Outline each uninfected red blood cell.
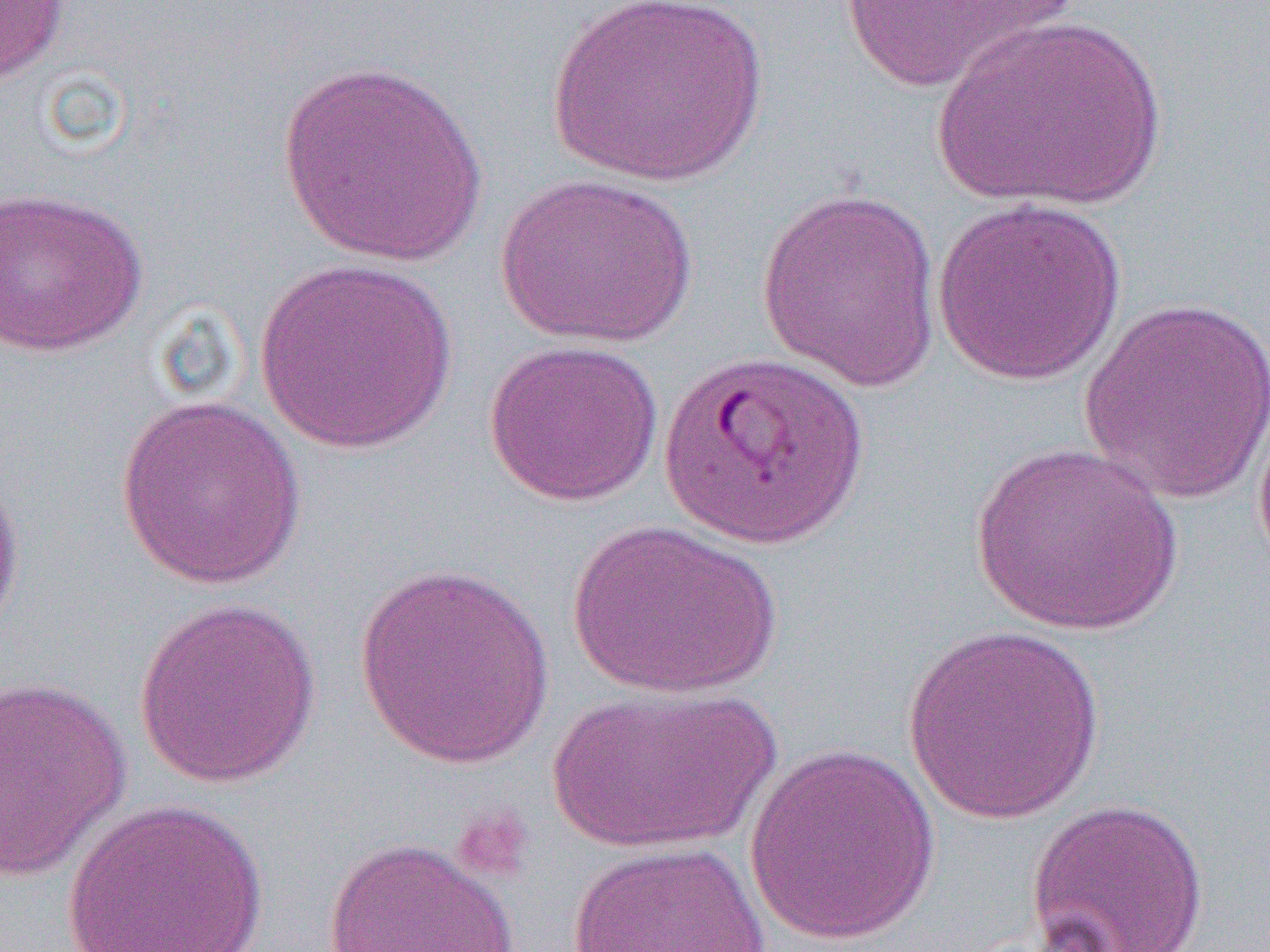

Approximate bounding boxes as named x1/y1/x2/y2 corners in pixels.
Uninfected red blood cells: (x1=0, y1=0, x2=71, y2=88), (x1=546, y1=0, x2=769, y2=186), (x1=833, y1=0, x2=1080, y2=95), (x1=932, y1=15, x2=1167, y2=211), (x1=274, y1=60, x2=493, y2=267), (x1=495, y1=172, x2=699, y2=349), (x1=0, y1=185, x2=149, y2=357), (x1=756, y1=188, x2=942, y2=391), (x1=931, y1=196, x2=1127, y2=387), (x1=253, y1=259, x2=459, y2=454), (x1=1078, y1=295, x2=1270, y2=505), (x1=484, y1=339, x2=665, y2=507), (x1=1251, y1=388, x2=1270, y2=587), (x1=114, y1=393, x2=309, y2=589), (x1=970, y1=442, x2=1186, y2=636), (x1=0, y1=463, x2=25, y2=645), (x1=566, y1=518, x2=783, y2=698), (x1=353, y1=562, x2=556, y2=769), (x1=134, y1=596, x2=323, y2=790), (x1=901, y1=624, x2=1109, y2=824), (x1=0, y1=676, x2=132, y2=883), (x1=546, y1=685, x2=778, y2=854), (x1=743, y1=745, x2=941, y2=947), (x1=1024, y1=797, x2=1211, y2=951), (x1=61, y1=799, x2=270, y2=952), (x1=322, y1=836, x2=520, y2=952), (x1=566, y1=841, x2=770, y2=951).

{
  "slide_level_diagnosis": "Plasmodium falciparum",
  "preparation": "thin blood film",
  "platelet_locations": "approximate bounding boxes as named x1/y1/x2/y2 corners in pixels: (x1=449, y1=804, x2=535, y2=883)",
  "image_size": "1270×952 pixels",
  "field_of_view": "single",
  "magnification": "1000x",
  "modality": "optical microscopy"
}